Outline each blood parasite and name the species.
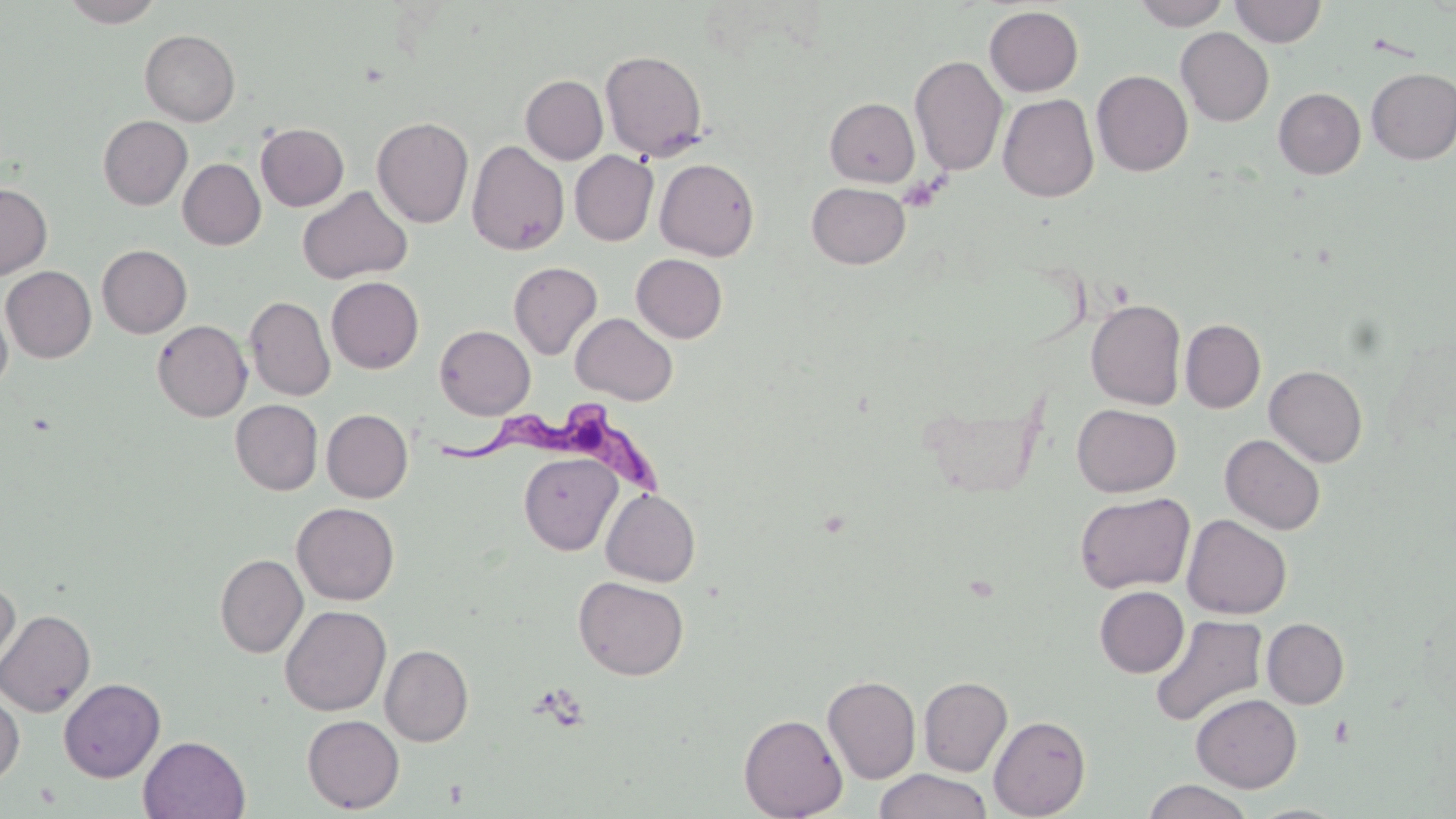

Approximate bounding boxes as (x1, y1, x2, y2) in pixels.
Trypanosoma brucei: (430, 403, 665, 499).
No Plasmodium falciparum, Plasmodium ovale, Plasmodium malariae, Plasmodium vivax, or Babesia divergens observed.

{
  "slide_level_diagnosis": "Trypanosoma brucei",
  "uninfected_red_blood_cell_locations": "approximate bounding boxes as (x1, y1, x2, y2) in pixels: (60, 0, 165, 27), (1132, 0, 1231, 30), (1230, 0, 1327, 47), (984, 6, 1083, 96), (1175, 27, 1274, 126), (140, 29, 240, 126), (600, 50, 708, 161), (909, 54, 1008, 176), (1366, 68, 1456, 164), (1091, 70, 1193, 176), (521, 74, 608, 164), (1273, 88, 1366, 179), (998, 93, 1098, 202), (825, 98, 920, 186), (98, 115, 192, 209), (372, 117, 474, 228), (256, 123, 349, 210), (467, 139, 569, 256), (570, 150, 659, 245), (654, 157, 759, 261), (178, 158, 266, 250), (806, 181, 911, 269), (0, 183, 52, 280), (297, 185, 413, 284), (97, 245, 192, 338), (631, 253, 728, 343), (508, 261, 603, 360), (1, 265, 97, 363), (326, 276, 424, 373), (244, 295, 335, 401), (0, 296, 13, 395), (1086, 298, 1186, 410), (570, 313, 678, 405), (1180, 319, 1266, 413), (152, 320, 252, 421), (435, 325, 535, 419), (1264, 364, 1367, 467), (230, 399, 323, 495), (1072, 404, 1181, 497), (322, 409, 413, 502), (1220, 434, 1326, 535), (519, 452, 621, 555), (601, 488, 701, 587), (1074, 492, 1195, 594), (291, 502, 400, 605), (1181, 514, 1292, 619), (215, 553, 308, 657), (0, 576, 20, 679), (573, 576, 689, 680), (1094, 586, 1189, 677), (280, 605, 391, 716), (0, 608, 96, 717), (1150, 614, 1268, 728), (1262, 618, 1349, 708), (380, 644, 473, 746), (822, 675, 921, 784), (919, 676, 1012, 777), (59, 678, 165, 782), (0, 688, 24, 786), (1191, 693, 1302, 792), (302, 714, 404, 813), (739, 714, 847, 819), (988, 715, 1091, 818), (138, 735, 250, 819), (873, 769, 993, 819), (1142, 779, 1254, 819)",
  "magnification": "1000x",
  "stain": "May-Grünwald-Giemsa",
  "field_of_view": "single",
  "modality": "light microscopy",
  "image_size": "1456×819 pixels",
  "preparation": "thin blood smear",
  "platelet_locations": "approximate bounding boxes as (x1, y1, x2, y2) in pixels: (897, 175, 943, 213)"
}